Comment on the morphology of the red blood cells.
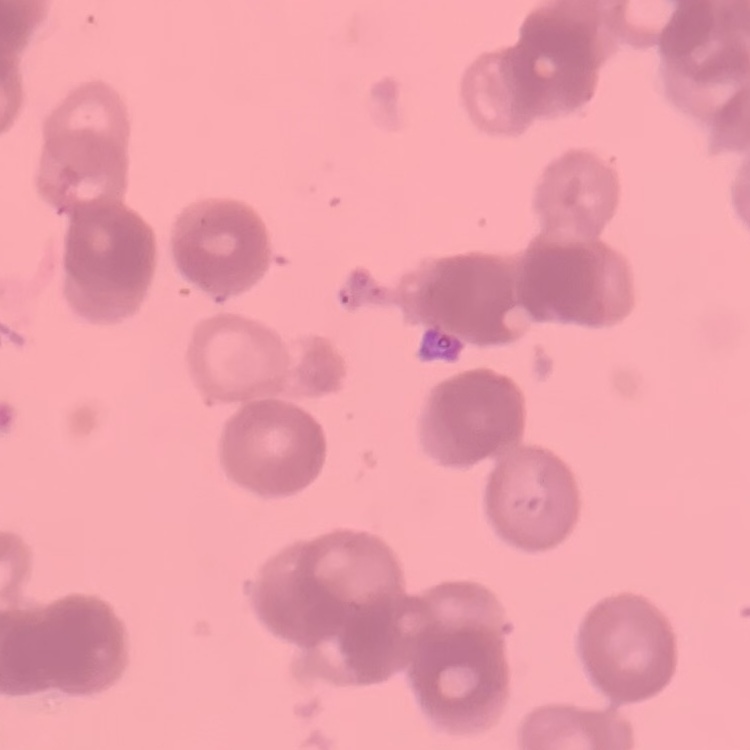

They show rouleaux formation.

{
  "image_type": "one tile cut from a larger photomicrograph",
  "preparation": "thin blood smear",
  "stain": "Field's or Giemsa"
}